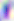
Summary:
  - Identification: Toxoplasma gondii
  - Magnification: 400x
  - Modality: photomicrograph